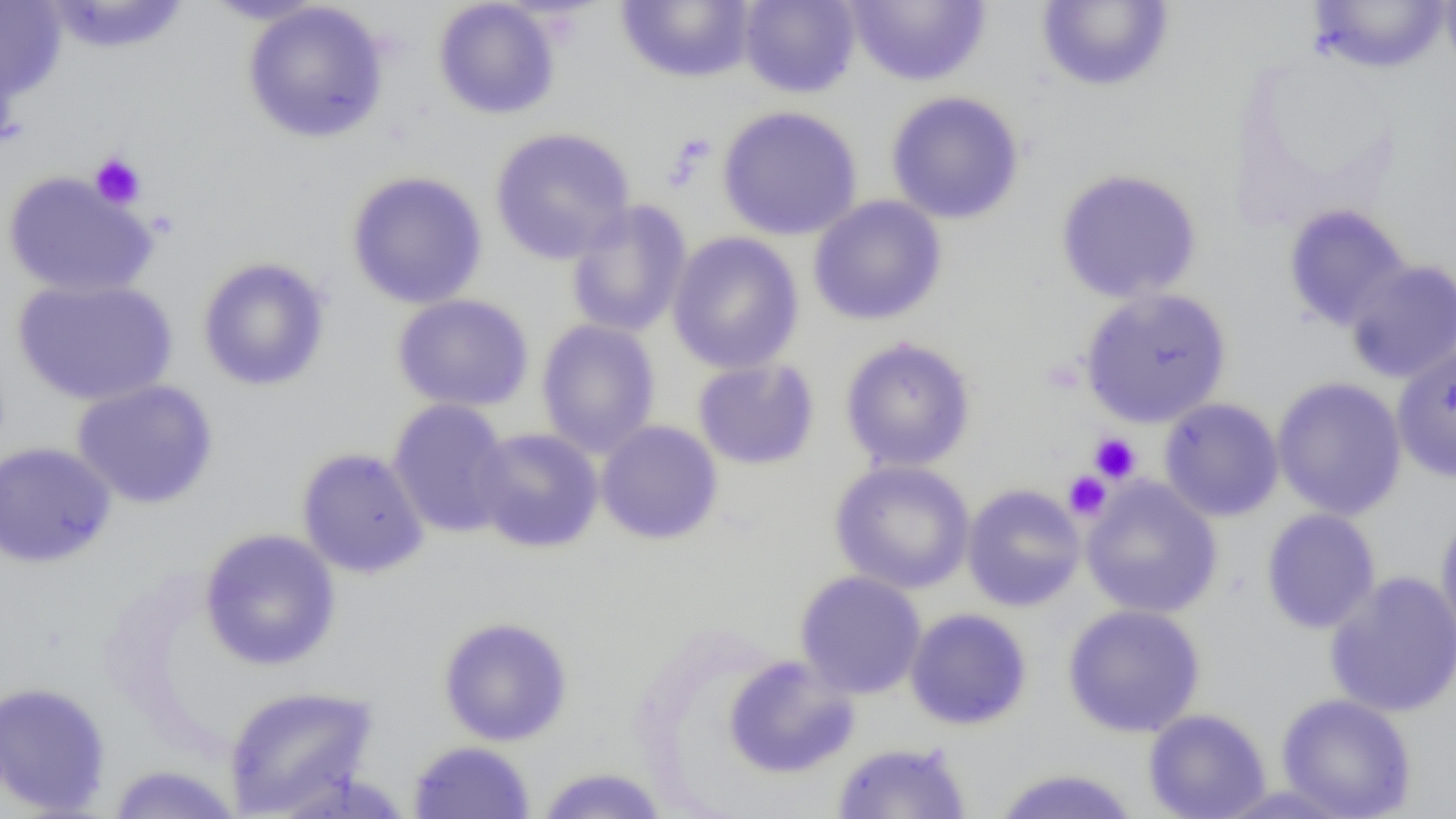 Approximate bounding boxes as (x1, y1, x2, y2) in pixels. Uninfected red blood cell locations: (39, 0, 193, 55), (201, 0, 329, 26), (433, 0, 561, 120), (738, 0, 861, 98), (844, 0, 992, 87), (1439, 0, 1456, 81), (0, 1, 66, 102), (242, 1, 389, 143), (616, 1, 757, 84), (1035, 1, 1176, 93), (1306, 1, 1453, 75), (885, 90, 1025, 225), (717, 105, 863, 241), (489, 127, 635, 265), (1055, 168, 1202, 304), (1, 170, 158, 299), (345, 170, 488, 310), (808, 195, 947, 326), (564, 200, 693, 339), (1282, 204, 1412, 333), (667, 231, 804, 374), (196, 256, 331, 392), (1344, 259, 1456, 384), (12, 277, 178, 406), (1079, 287, 1232, 428), (391, 293, 534, 412), (536, 319, 661, 458), (839, 336, 977, 472), (1391, 341, 1456, 483), (692, 358, 820, 470), (1271, 376, 1407, 521), (71, 379, 219, 509), (1158, 397, 1284, 522), (387, 398, 514, 539), (595, 420, 723, 545), (471, 427, 604, 553), (0, 442, 117, 568), (296, 447, 430, 579), (829, 460, 976, 594), (1080, 477, 1223, 619), (961, 484, 1086, 612), (1261, 508, 1382, 634), (1435, 508, 1456, 654), (199, 528, 341, 671), (794, 570, 927, 699), (1324, 570, 1456, 719), (1062, 604, 1206, 738), (904, 608, 1032, 730), (437, 616, 573, 746), (722, 654, 860, 779), (0, 681, 112, 816), (223, 685, 379, 817), (1276, 693, 1417, 818), (1143, 708, 1272, 819), (407, 740, 536, 818), (831, 741, 972, 818), (105, 764, 242, 818), (534, 767, 670, 818), (989, 767, 1142, 818). Platelet locations: (89, 153, 146, 210), (1089, 433, 1141, 483), (1062, 471, 1111, 521). Slide-level diagnosis: negative for blood parasites. Light microscopy. Captured at 1000x magnification. Image is 1456×819 pixels. Thin blood smear. Single field of view.